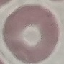
Summary:
  - Result: no malaria parasites detected
  - Image type: cell patch, automatically extracted from a larger field of view and resized to 64 × 64 pixels
  - Capture: smartphone camera at the microscope eyepiece
  - Stain: Giemsa
  - Preparation: thin blood film